Report the malaria status of this cell.
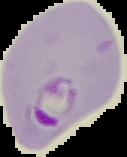

It is parasitized.

From a thin blood smear. Image is 127×157 pixels. Cell region segmented out of the field of view; the surrounding area is masked to black.